Assess this cell for malaria.
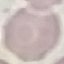

It is uninfected.

Summary:
  - Stain: Giemsa
  - Preparation: thin blood smear
  - Capture: smartphone through the microscope eyepiece
  - Image type: cell patch, automatically extracted from a larger field of view and resized to 64 × 64 pixels